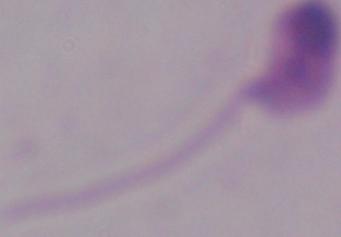

Summary:
  - Magnification: 1000x
  - Identification: Leishmania
  - Modality: micrograph